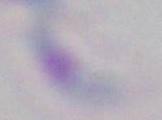 Photomicrograph. Toxoplasma gondii is shown. 1000x magnification.